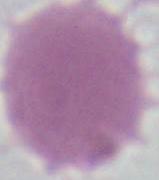
Summary:
  - Magnification: 1000x
  - Identification: red blood cell
  - Modality: micrograph